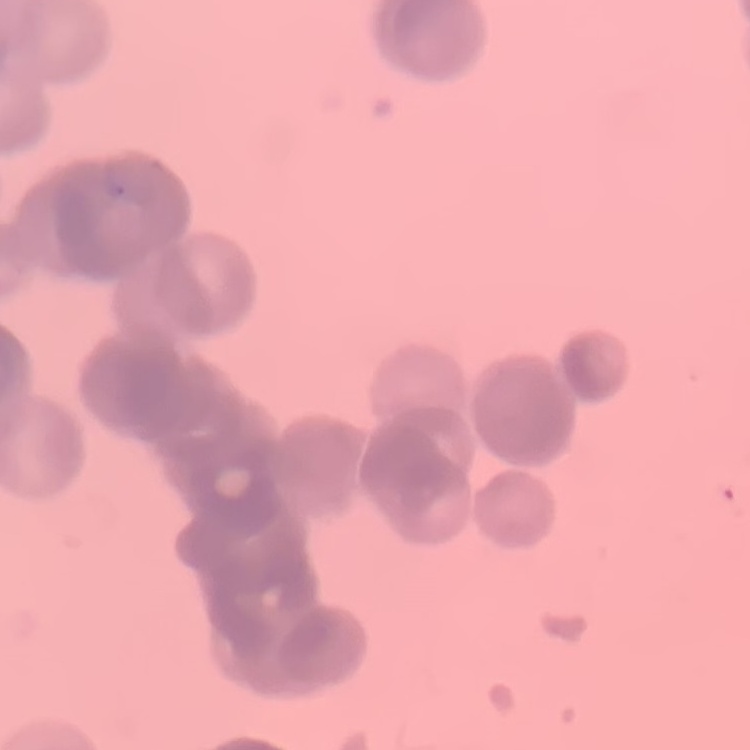 The erythrocytes exhibit rouleaux formation. Thin peripheral smear. One tile cut from a larger photomicrograph. Stained with either Field's or Giemsa.